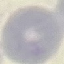
{
  "result": "no malaria parasites seen",
  "preparation": "thin blood film",
  "image_type": "cell patch, automatically extracted from a larger field of view and resized to 64 × 64 pixels",
  "capture": "smartphone camera at the microscope eyepiece",
  "stain": "Giemsa"
}